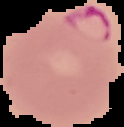
From a thin blood smear. Result: malaria parasites detected. Image is 124×127 pixels. The area outside the segmented cell region is set to black.